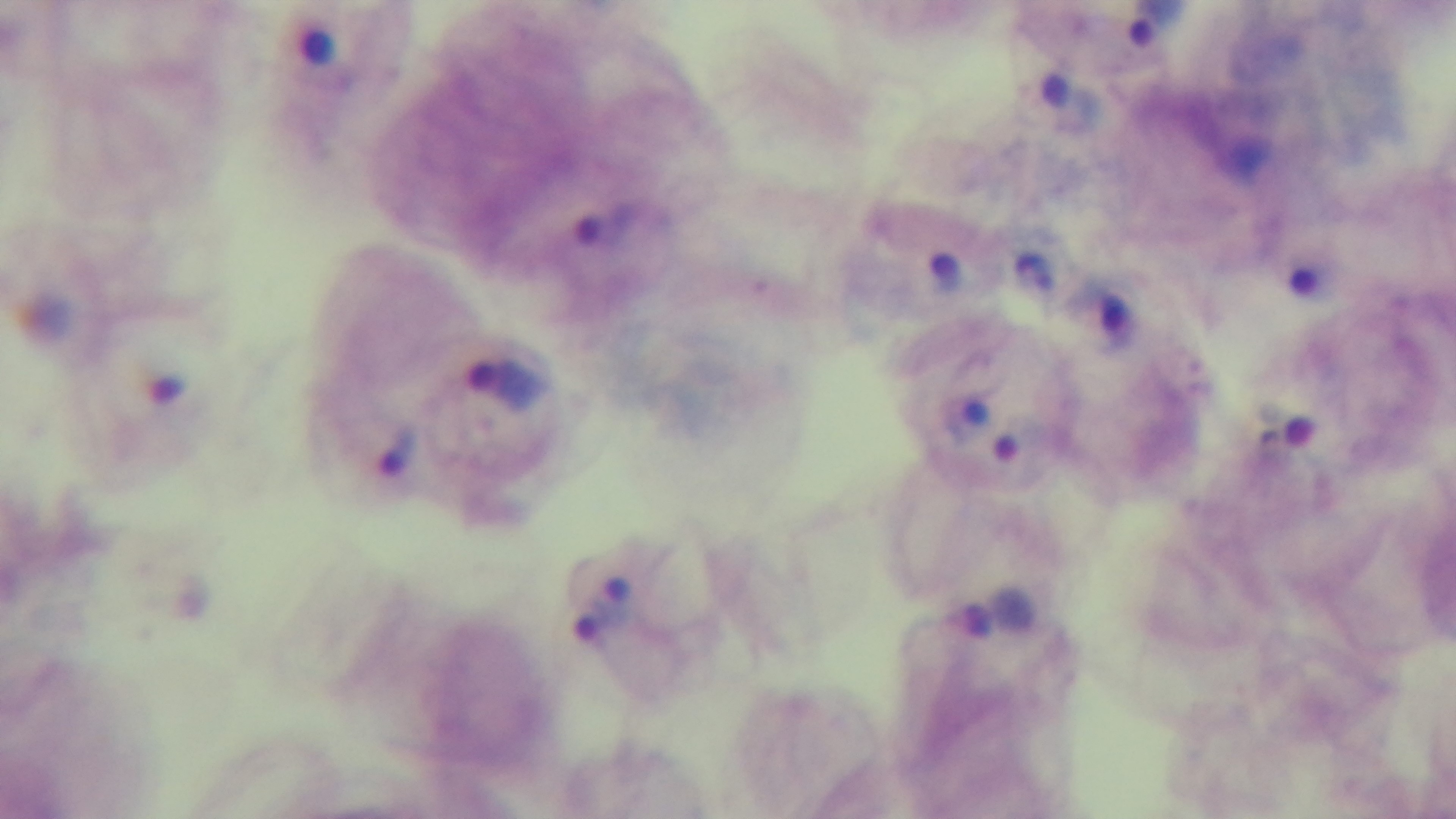 100x oil-immersion objective. Photomicrograph. Giemsa-stained. Malaria status: infected. Single field of view. Preparation: thick blood film. Mounted 4K digital camera.